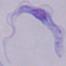

{
  "modality": "micrograph",
  "identification": "trypanosome",
  "magnification": "1000x"
}